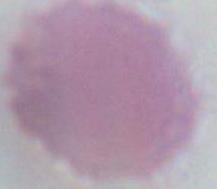
Summary:
  - Modality: micrograph
  - Identification: red blood cell
  - Magnification: 1000x